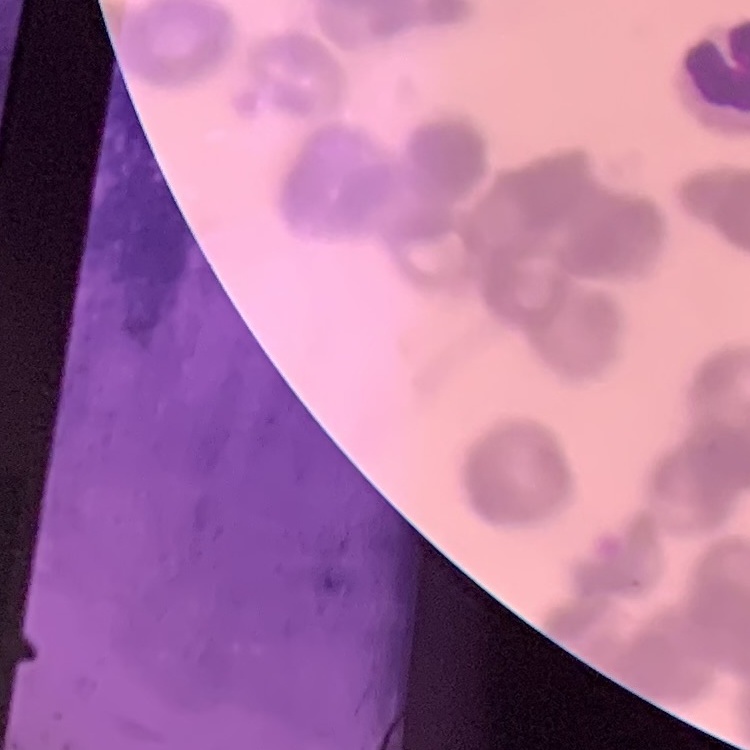 The red blood cells show rouleaux formation. Thin blood smear. One tile cut from a larger photomicrograph. Stained with either Field's or Giemsa.